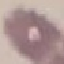
Summary:
  - Malaria status: uninfected
  - Stain: Giemsa
  - Image type: cell patch, automatically extracted from a larger field of view and resized to 64 × 64 pixels
  - Preparation: thin smear
  - Capture: smartphone camera at the microscope eyepiece